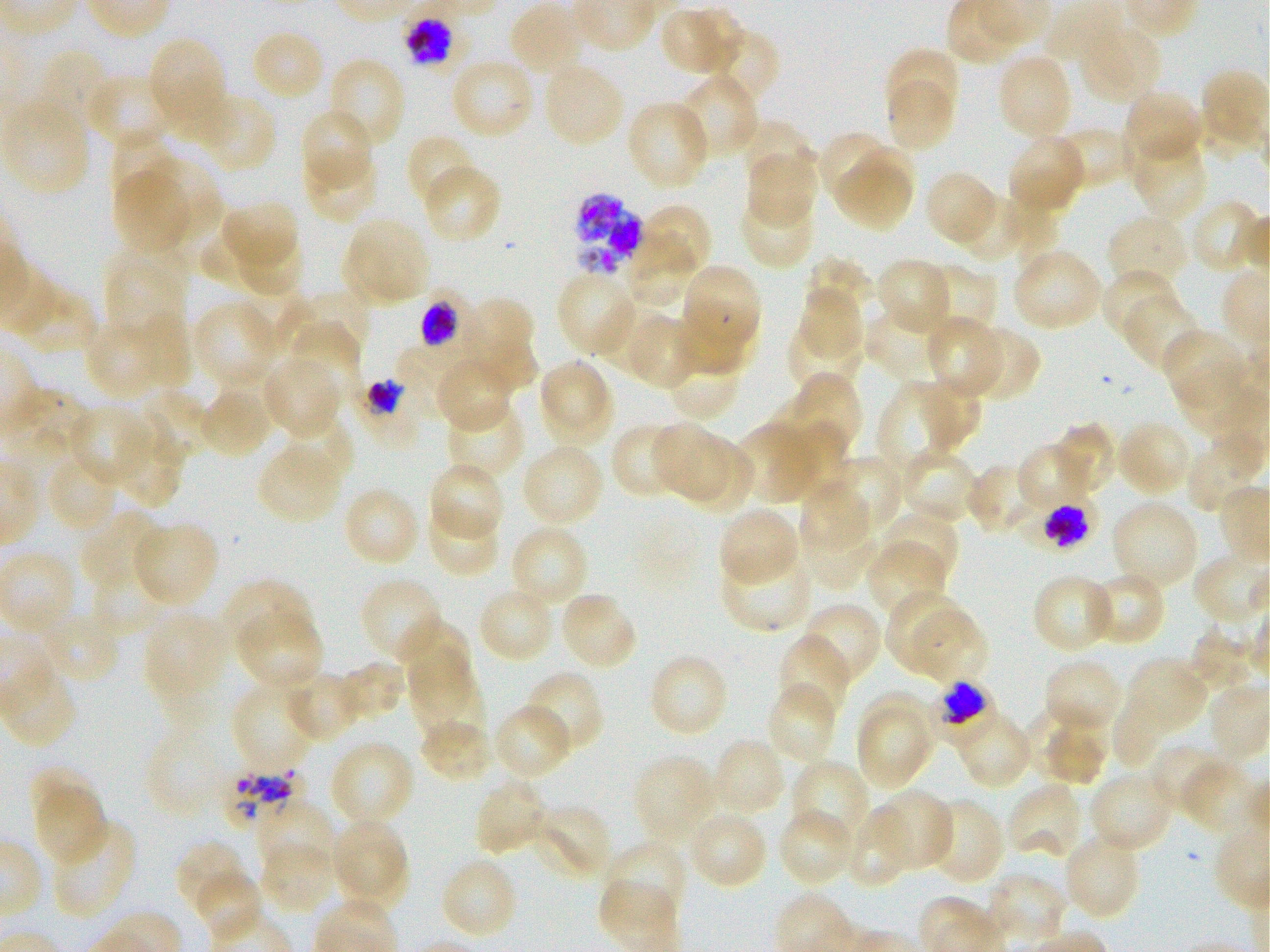

Approximate bounding boxes as {x1, y1, x2, y2} in pixels. Not every red blood cell is marked. A life-cycle stage — or a range of stages, where the recorded stages span more than one — follows each staged infected red blood cell. Locations of uninfected red blood cells: {508, 3, 585, 77}, {682, 4, 748, 77}, {662, 10, 720, 74}, {1079, 24, 1163, 102}, {703, 27, 781, 108}, {256, 34, 322, 95}, {151, 41, 220, 120}, {885, 47, 960, 123}, {36, 48, 111, 137}, {996, 53, 1073, 140}, {328, 56, 406, 150}, {449, 57, 536, 140}, {542, 62, 626, 147}, {678, 73, 760, 159}, {85, 74, 170, 148}, {885, 79, 954, 152}, {167, 86, 237, 146}, {1123, 91, 1203, 168}, {206, 95, 272, 171}, {4, 99, 89, 197}, {625, 99, 710, 191}, {300, 107, 372, 187}, {737, 120, 816, 187}, {1052, 126, 1132, 190}, {817, 131, 896, 203}, {406, 133, 478, 209}, {110, 134, 181, 210}, {1007, 135, 1086, 214}, {1130, 136, 1208, 221}, {848, 146, 914, 204}, {303, 149, 378, 223}, {746, 151, 818, 228}, {144, 155, 221, 240}, {422, 163, 500, 244}, {836, 166, 910, 232}, {113, 170, 187, 255}, {925, 170, 998, 244}, {953, 190, 1028, 262}, {739, 194, 815, 270}, {1190, 199, 1264, 276}, {223, 200, 298, 267}, {640, 202, 712, 278}, {1006, 203, 1058, 260}, {1106, 214, 1188, 292}, {343, 216, 431, 305}, {200, 227, 272, 289}, {627, 230, 697, 306}, {232, 236, 300, 295}, {1012, 248, 1103, 333}, {103, 253, 186, 339}, {804, 255, 876, 323}, {875, 258, 952, 335}, {923, 263, 997, 337}, {684, 268, 759, 349}, {1100, 268, 1176, 342}, {555, 271, 637, 357}, {799, 284, 863, 363}, {298, 288, 370, 360}, {1125, 293, 1201, 372}, {464, 298, 537, 387}, {194, 300, 279, 387}, {866, 305, 946, 382}, {132, 311, 193, 388}, {621, 313, 701, 389}, {680, 314, 758, 374}, {785, 316, 862, 398}, {924, 317, 1003, 399}, {85, 321, 164, 399}, {288, 321, 361, 404}, {964, 326, 1042, 403}, {1162, 328, 1248, 409}, {476, 338, 537, 392}, {396, 342, 476, 405}, {665, 349, 737, 421}, {435, 355, 513, 431}, {261, 358, 340, 438}, {538, 360, 615, 444}, {1173, 367, 1253, 435}, {791, 374, 862, 454}, {915, 377, 982, 451}, {442, 381, 522, 454}, {878, 384, 956, 477}, {199, 387, 273, 458}, {128, 389, 209, 463}, {766, 391, 834, 458}, {445, 401, 525, 482}, {69, 405, 151, 486}, {114, 413, 192, 510}, {281, 416, 354, 487}, {1116, 419, 1192, 497}, {789, 420, 860, 506}, {612, 422, 686, 500}, {1056, 422, 1116, 495}, {736, 423, 819, 504}, {652, 426, 733, 501}, {1185, 434, 1264, 515}, {677, 436, 756, 513}, {1018, 442, 1092, 510}, {520, 443, 605, 526}, {257, 446, 341, 524}, {900, 448, 978, 525}, {46, 452, 121, 533}, {827, 455, 901, 538}, {428, 461, 505, 541}, {965, 461, 1041, 536}, {800, 479, 868, 555}, {342, 486, 421, 568}, {1111, 500, 1200, 590}, {427, 505, 501, 578}, {718, 507, 801, 586}, {881, 510, 960, 586}, {82, 511, 165, 592}, {134, 521, 219, 606}, {800, 523, 876, 589}, {509, 524, 590, 608}, {868, 540, 946, 620}, {720, 549, 813, 632}, {1086, 570, 1167, 646}, {1031, 573, 1115, 654}, {93, 574, 164, 637}, {361, 577, 445, 663}, {221, 579, 312, 655}, {477, 585, 555, 664}, {886, 588, 972, 673}, {560, 592, 638, 671}, {800, 602, 881, 685}, {907, 606, 987, 684}, {39, 611, 121, 686}, {143, 611, 229, 697}, {237, 612, 323, 690}, {397, 618, 470, 689}, {777, 634, 850, 722}, {401, 644, 479, 720}, {647, 652, 730, 739}, {1125, 657, 1208, 734}, {1043, 658, 1119, 727}, {338, 662, 405, 722}, {408, 665, 484, 743}, {2, 666, 76, 749}, {282, 669, 360, 742}, {524, 669, 606, 754}, {231, 681, 315, 772}, {765, 684, 837, 765}, {861, 690, 940, 767}, {1111, 696, 1169, 769}, {492, 704, 574, 781}, {1022, 707, 1109, 780}, {856, 710, 928, 789}, {958, 714, 1032, 788}, {419, 718, 492, 784}, {1042, 726, 1105, 786}, {149, 731, 221, 815}, {711, 737, 786, 816}, {329, 739, 416, 827}, {1147, 744, 1226, 815}, {632, 754, 717, 843}, {1182, 758, 1257, 835}, {790, 759, 870, 845}, {29, 766, 97, 825}, {1088, 770, 1173, 854}, {474, 777, 551, 857}, {1005, 782, 1084, 861}, {33, 784, 105, 868}, {873, 790, 952, 873}, {928, 797, 1006, 885}, {254, 800, 335, 877}, {531, 803, 612, 881}, {778, 808, 856, 888}, {845, 808, 916, 888}, {688, 809, 769, 890}, {331, 818, 407, 895}, {50, 819, 137, 920}, {1062, 833, 1142, 920}, {174, 840, 246, 914}, {259, 842, 337, 915}, {338, 842, 410, 907}, {600, 842, 687, 923}, {440, 857, 519, 941}, {195, 871, 264, 942}, {985, 872, 1068, 945}. Locations of red blood cells of indeterminate infection status: {401, 2, 470, 73}, {1017, 492, 1098, 549}, {936, 681, 994, 740}, {221, 763, 305, 827}. Locations of infected red blood cells: {573, 193, 645, 277}; {420, 287, 470, 356} early trophozoite to early schizont; {356, 378, 417, 445} trophozoite. Giemsa-stained preparation. One field from this slide. Donor blood group O+. Thin blood smear. 100x oil-immersion objective, numerical aperture 1.25. Static in-vitro culture of Plasmodium falciparum strain 3D7. Image is 1270×952 pixels.